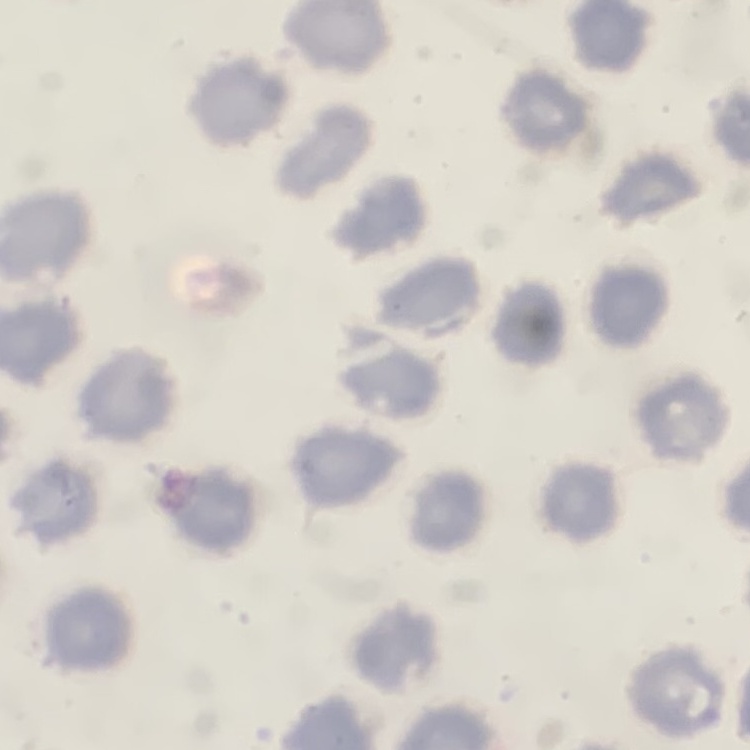
The red blood cells exhibit no rouleaux formation. Thin blood smear. Square crop of a larger photomicrograph. Field's or Giemsa stain.